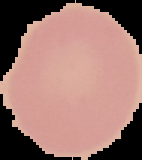 Image is 142×160 pixels. Result: negative for Plasmodium parasites. The area outside the segmented cell region is set to black. From a thin blood smear.